Assess for Plasmodium parasites.
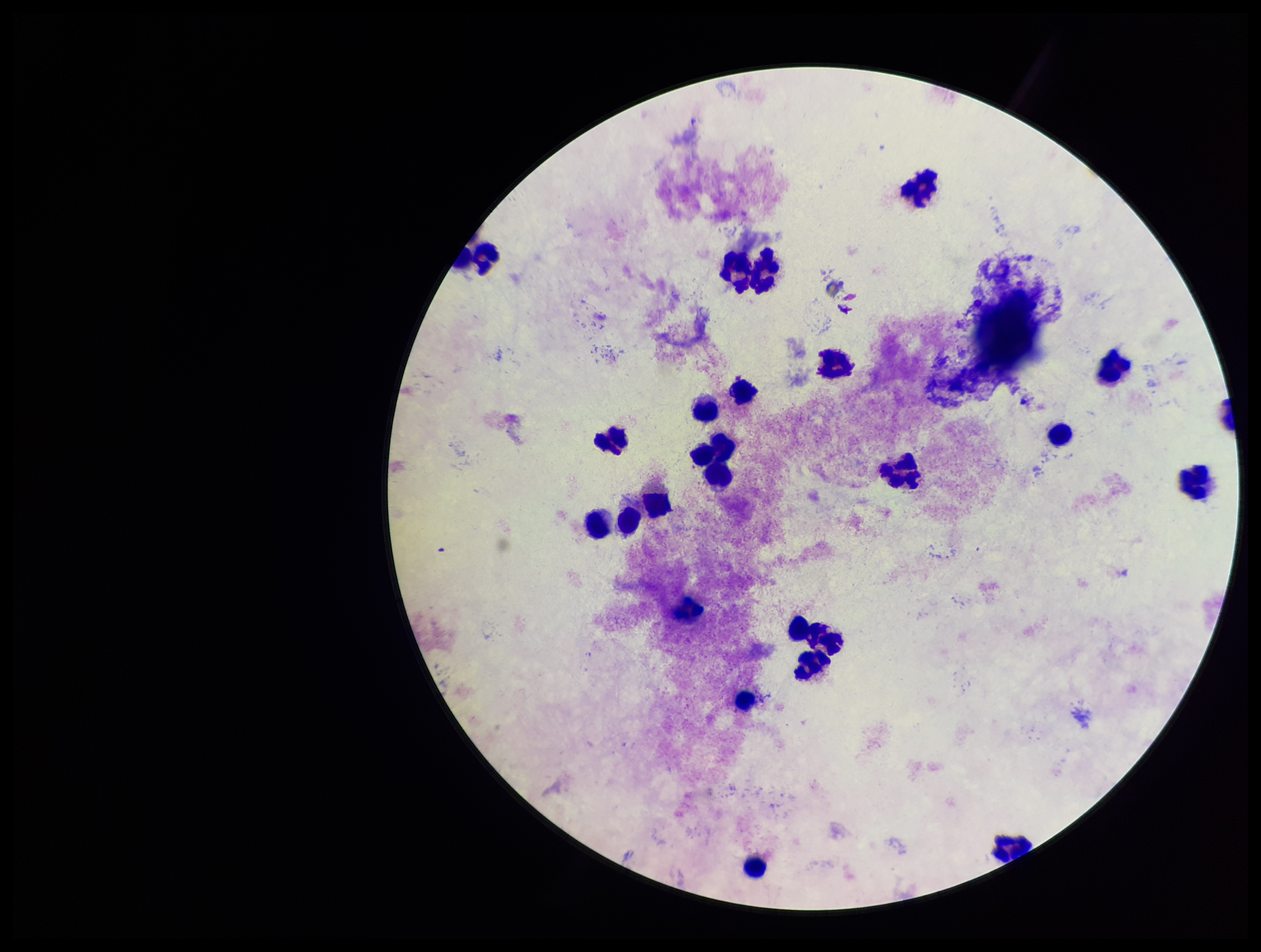
None detected.

One field from this slide. Giemsa stain. Preparation: thick smear. Image is 1261×952 pixels. Leukocyte count: 26. Parasite count: 0. Smartphone photograph taken through the eyepiece of a microscope. Patient malaria status: negative.